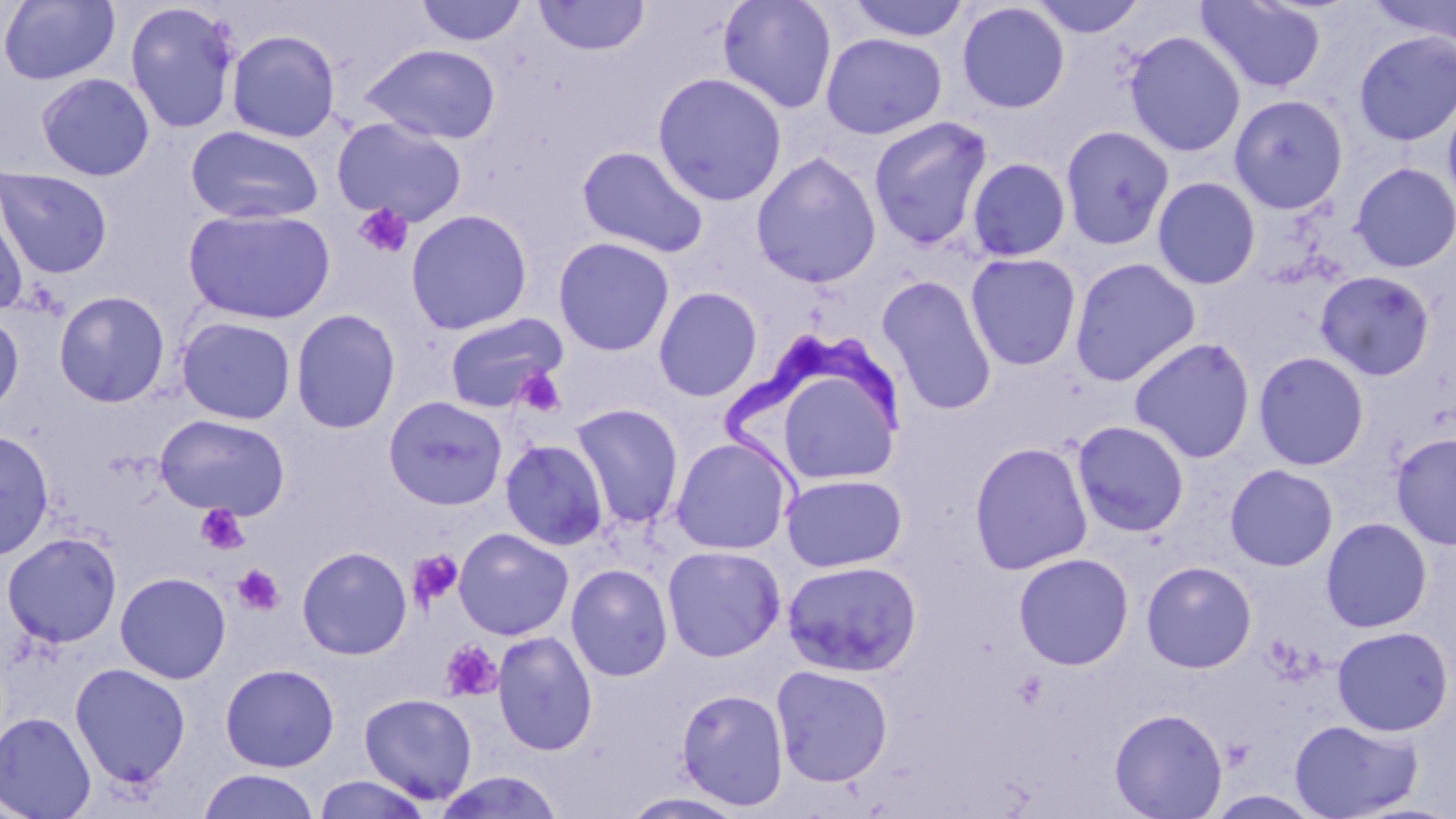
Summary:
  - Coordinate format: approximate bounding boxes as [x1, y1, x2, y2] in pixels
  - Trypanosoma brucei locations: [723, 325, 904, 495]
  - Platelet locations: [353, 203, 415, 259], [515, 367, 567, 418], [196, 505, 250, 555], [407, 549, 464, 609], [232, 564, 284, 616], [439, 639, 503, 702]
  - Uninfected red blood cell locations: [414, 0, 529, 48], [533, 0, 650, 57], [717, 0, 838, 114], [846, 0, 970, 43], [1027, 0, 1148, 38], [1195, 0, 1328, 95], [1367, 0, 1456, 47], [0, 1, 120, 86], [124, 2, 242, 134], [956, 2, 1070, 114], [226, 29, 341, 143], [1124, 30, 1246, 158], [1353, 30, 1456, 146], [820, 32, 947, 140], [360, 43, 502, 145], [652, 71, 788, 207], [35, 73, 155, 181], [1442, 87, 1456, 217], [1228, 94, 1349, 214], [867, 115, 994, 250], [332, 117, 468, 226], [1060, 124, 1175, 250], [185, 125, 324, 225], [576, 145, 709, 259], [751, 151, 882, 288], [966, 158, 1072, 262], [1350, 162, 1456, 272], [0, 169, 113, 278], [1152, 176, 1261, 290], [0, 196, 29, 317], [182, 207, 336, 325], [405, 208, 532, 335], [552, 236, 675, 357], [965, 252, 1082, 371], [1069, 257, 1202, 386], [1315, 270, 1435, 380], [877, 275, 997, 416], [653, 286, 762, 402], [53, 290, 171, 407], [290, 308, 401, 433], [0, 311, 24, 418], [442, 312, 568, 414], [175, 316, 297, 425], [1128, 337, 1256, 464], [1253, 351, 1370, 471], [383, 396, 508, 510], [570, 403, 684, 530], [155, 414, 290, 519], [1071, 420, 1190, 537], [0, 430, 55, 561], [1391, 431, 1456, 551], [670, 436, 794, 555], [500, 438, 609, 550], [969, 441, 1093, 575], [1225, 464, 1339, 571], [780, 473, 908, 571], [1321, 517, 1433, 633], [453, 527, 574, 640], [1, 532, 122, 648], [296, 545, 413, 660], [662, 545, 785, 662], [1012, 552, 1134, 670], [781, 560, 922, 677], [1141, 561, 1257, 673], [566, 563, 673, 682], [115, 571, 232, 684], [1332, 625, 1454, 736], [492, 630, 598, 756], [69, 662, 191, 789], [219, 663, 340, 772], [770, 664, 894, 787], [676, 687, 790, 810], [358, 692, 478, 805], [1108, 707, 1228, 819], [1, 711, 96, 819], [1289, 718, 1423, 819], [197, 769, 321, 819], [431, 770, 567, 818], [312, 774, 432, 818], [620, 792, 750, 818]
  - Slide-level diagnosis: Trypanosoma brucei
  - Magnification: 1000x
  - Image size: 1456×819 pixels
  - Stain: May-Grünwald-Giemsa
  - Preparation: thin blood film
  - Modality: light microscopy
  - Field of view: single